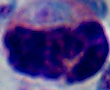

1000x magnification. Photomicrograph. A white blood cell is shown.